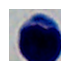

Summary:
  - Identification: leukocyte
  - Magnification: 1000x
  - Modality: photomicrograph